Describe the morphology of the red blood cells.
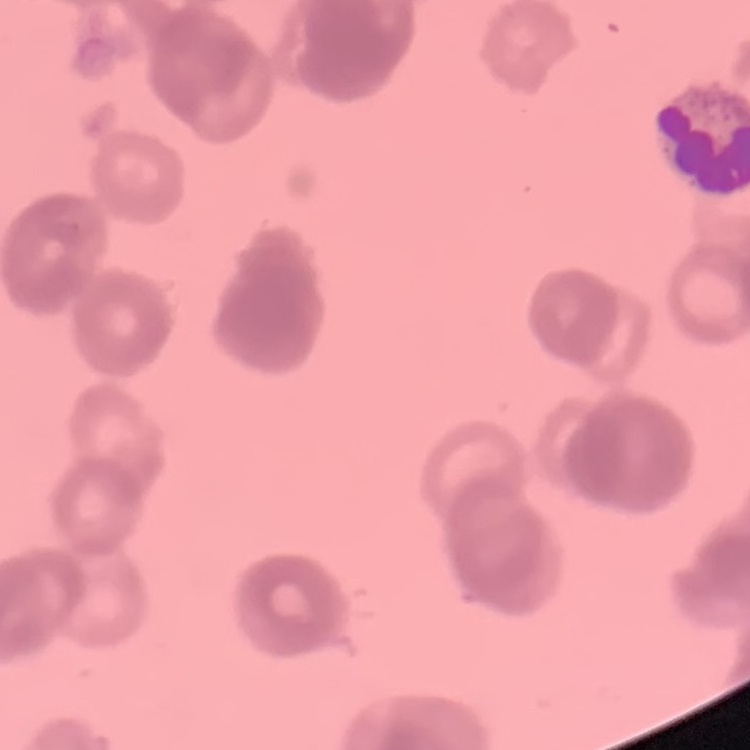

Rouleaux formation.

image type = square crop of a larger photomicrograph
preparation = thin blood film
stain = Field's or Giemsa